Look for Plasmodium parasites.
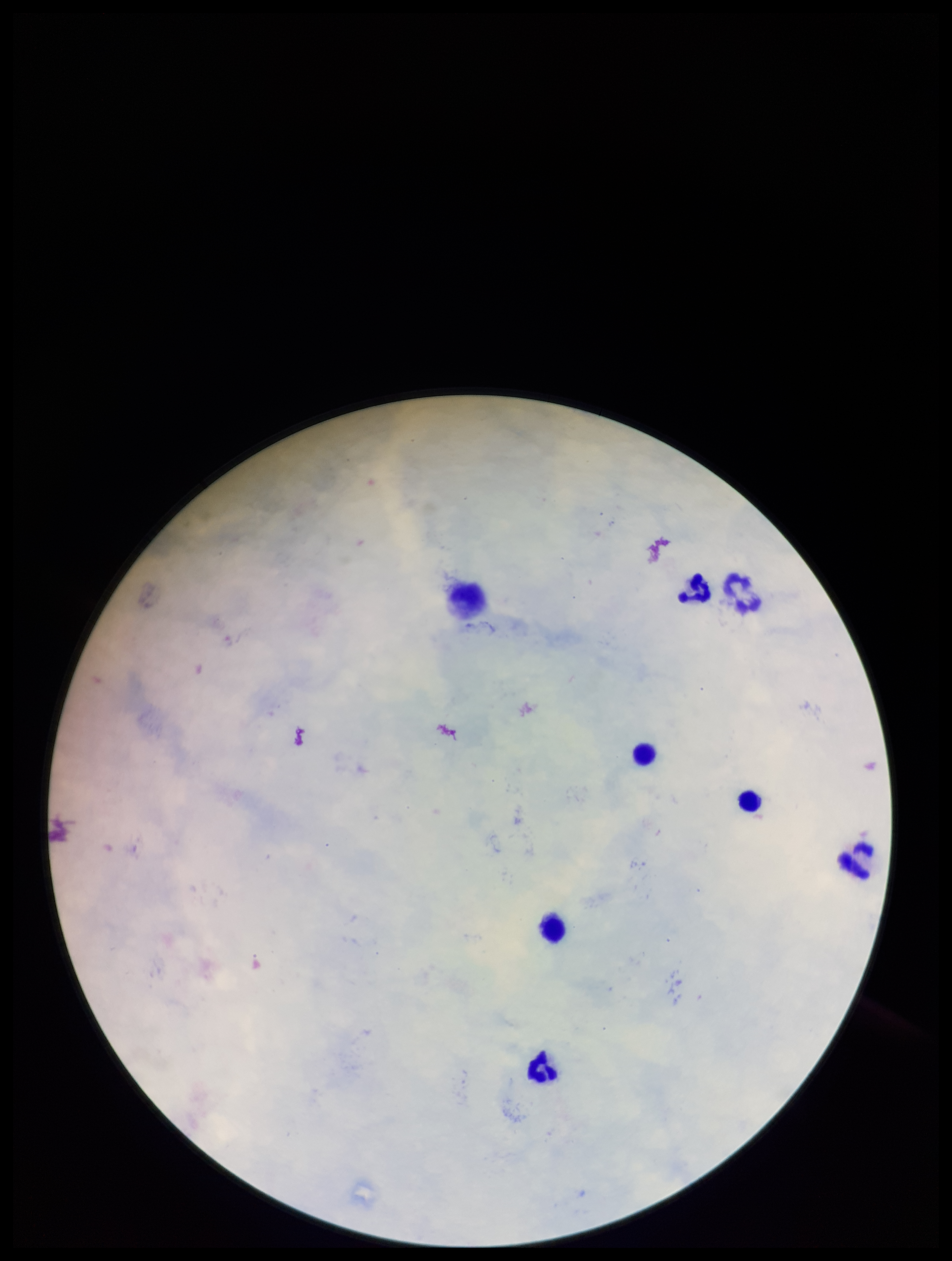

None seen.

field of view = single
patient malaria status = negative
parasite count = 0
capture = smartphone photograph through the microscope eyepiece
leukocyte count = 6
preparation = thick smear
stain = Giemsa
image size = 952×1261 pixels